Describe the morphology of the red blood cells.
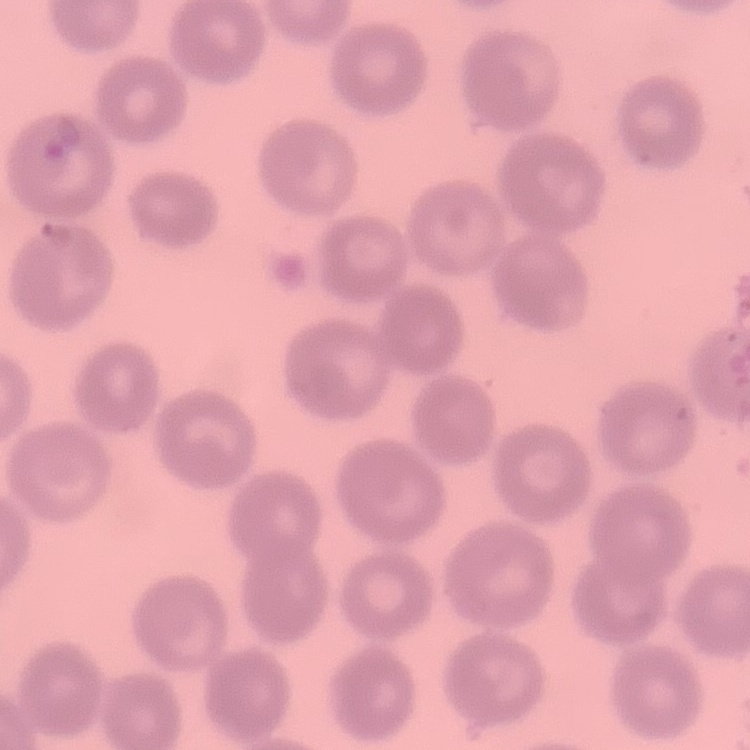

No rouleaux formation.

Summary:
  - Stain: Field's or Giemsa
  - Preparation: thin blood smear
  - Image type: square crop of a larger photomicrograph